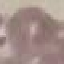

Summary:
  - Result: no malaria parasites seen
  - Capture: smartphone camera at the microscope eyepiece
  - Stain: Giemsa
  - Preparation: thin blood film
  - Image type: automatically extracted cell patch, resized to 64 × 64 pixels